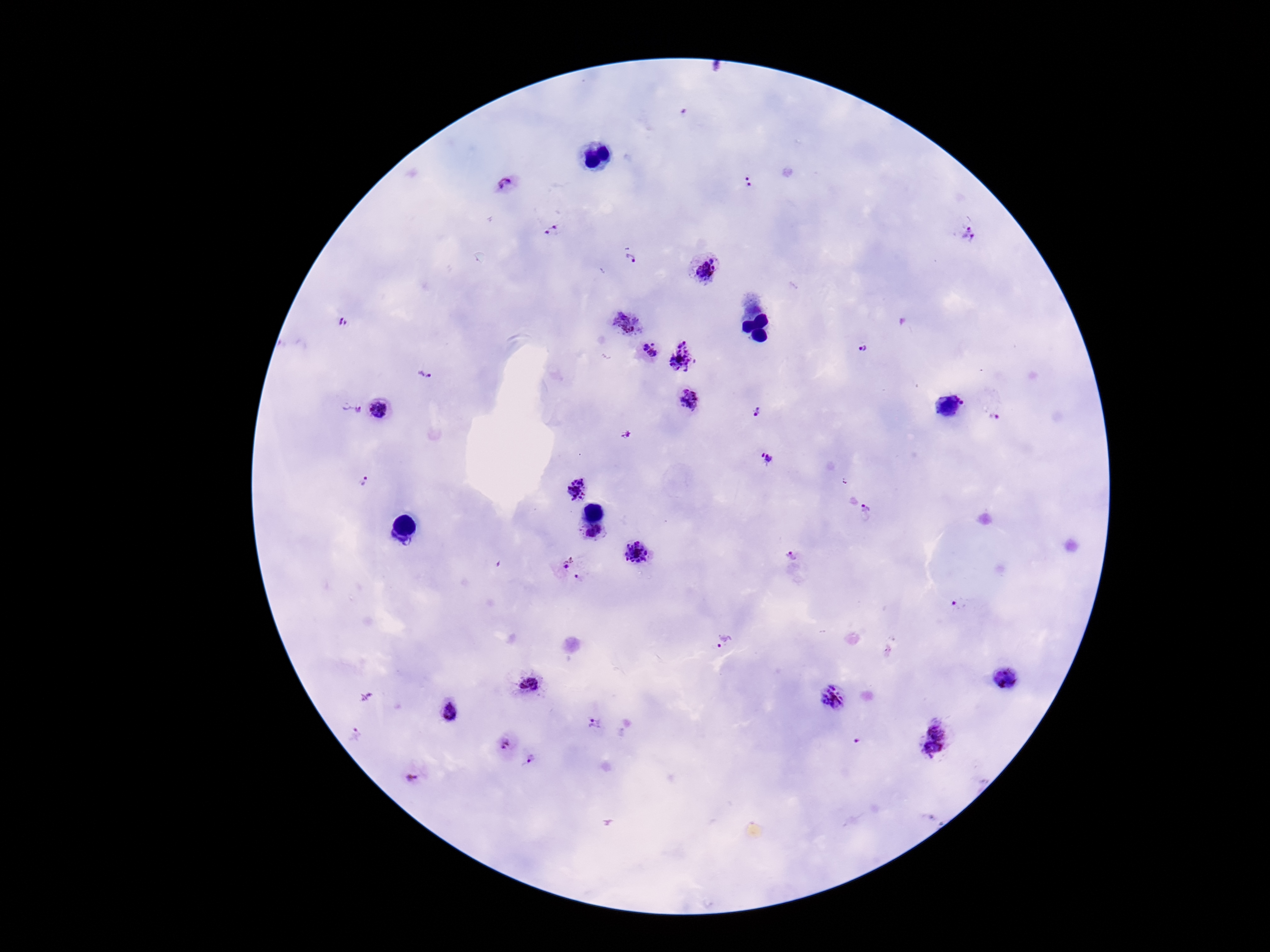
preparation = thick blood smear
capture = smartphone camera through the microscope eyepiece
magnification = 100x
image size = 1270×952 pixels
stain = Giemsa
field of view = one from this slide
patient malaria status = positive
Plasmodium parasite locations = approximate centers as (x, y) in pixels: (748, 181), (506, 185), (553, 230), (969, 232), (630, 261), (703, 272), (625, 320), (344, 325), (860, 348), (649, 352), (684, 354), (425, 374), (689, 401), (948, 407), (350, 410), (753, 410), (379, 412), (997, 417), (628, 435), (765, 457), (365, 481), (577, 488), (861, 508), (593, 535), (637, 553), (563, 559), (791, 561), (577, 578), (957, 607), (725, 643), (1007, 677), (532, 684), (833, 698), (447, 712), (597, 725), (938, 727), (504, 746), (932, 752), (530, 761), (412, 777)